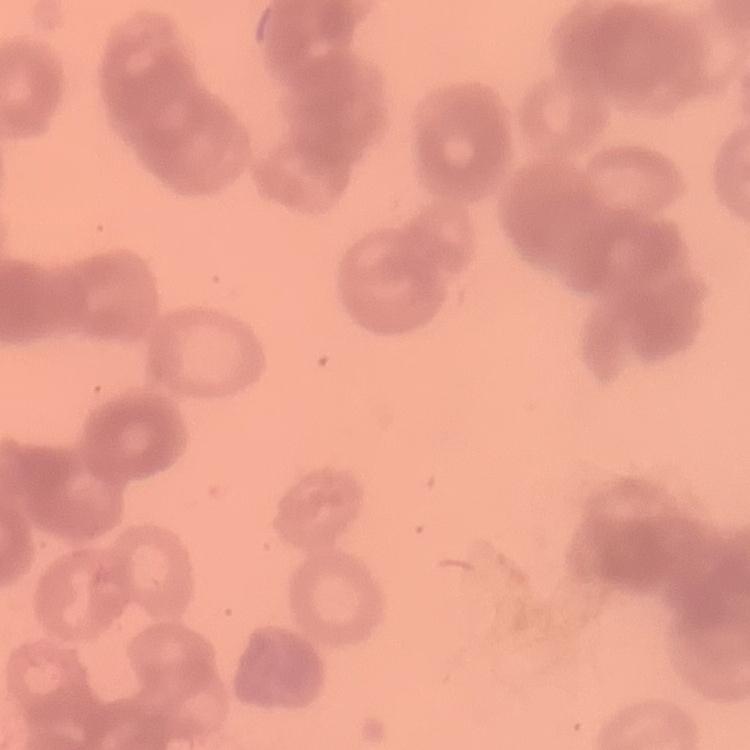

The erythrocytes exhibit rouleaux formation. Field's or Giemsa stain. Thin peripheral smear. Square crop of a larger photomicrograph.